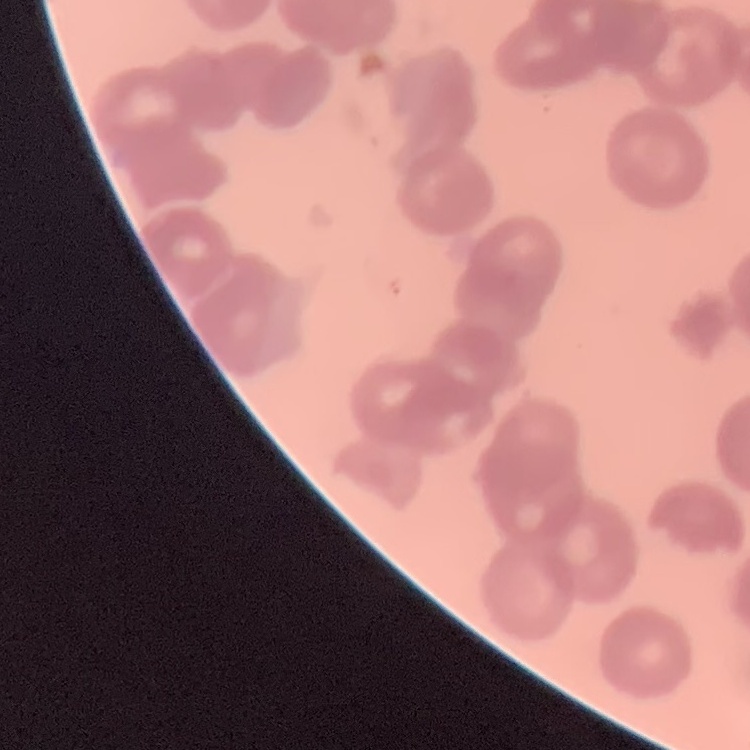 The erythrocytes show rouleaux formation. Thin peripheral smear. Field's or Giemsa stain. Square crop of a larger photomicrograph.